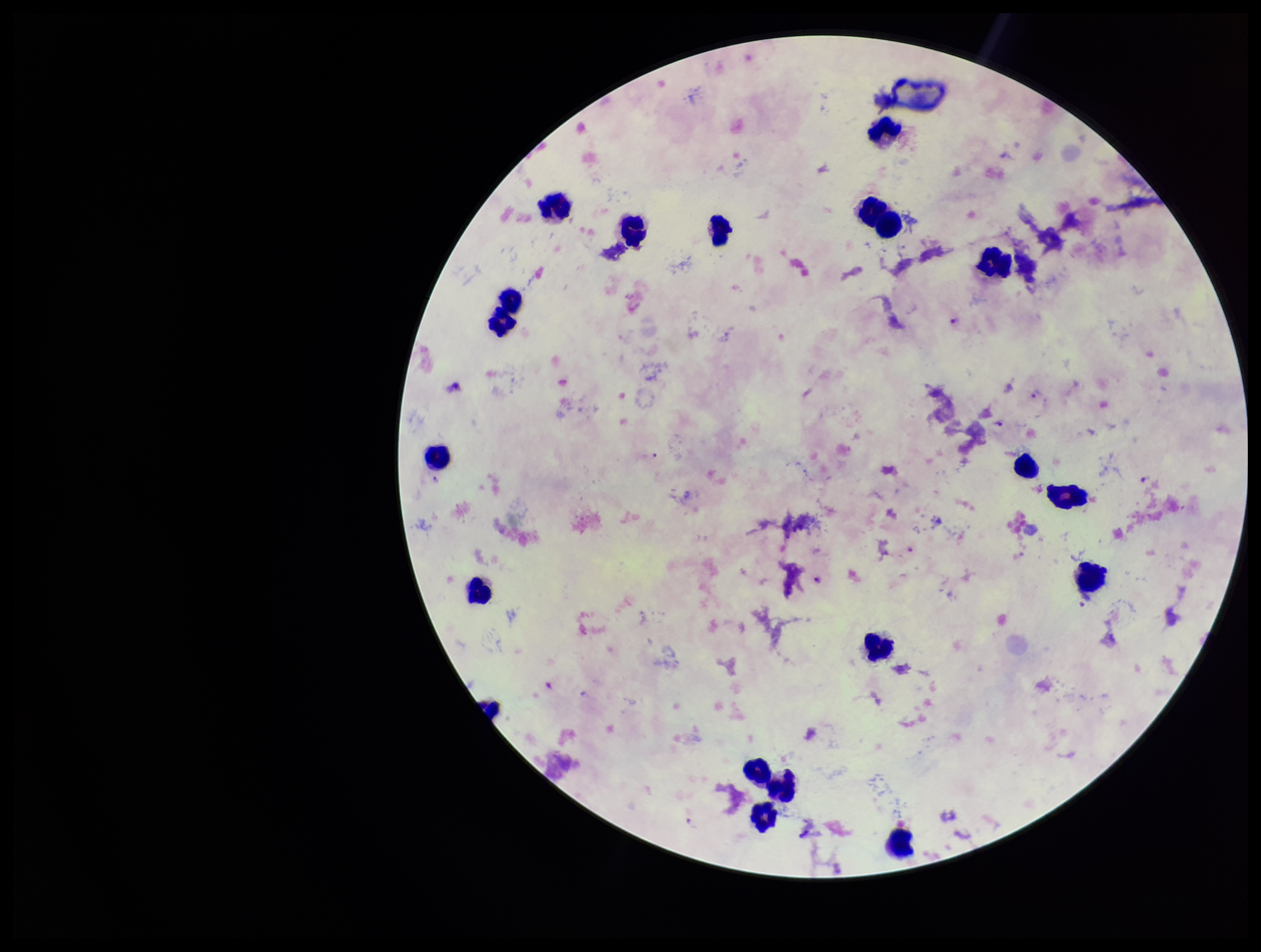
Summary:
  - Preparation: thick smear
  - Leukocyte count: 19
  - Species reported for this patient: Plasmodium falciparum
  - Stain: Giemsa
  - Parasite count: 5
  - Field of view: one from this slide
  - Patient malaria status: positive
  - Capture: smartphone photograph through the microscope eyepiece
  - Image size: 1261×952 pixels
  - Plasmodium parasites: detected